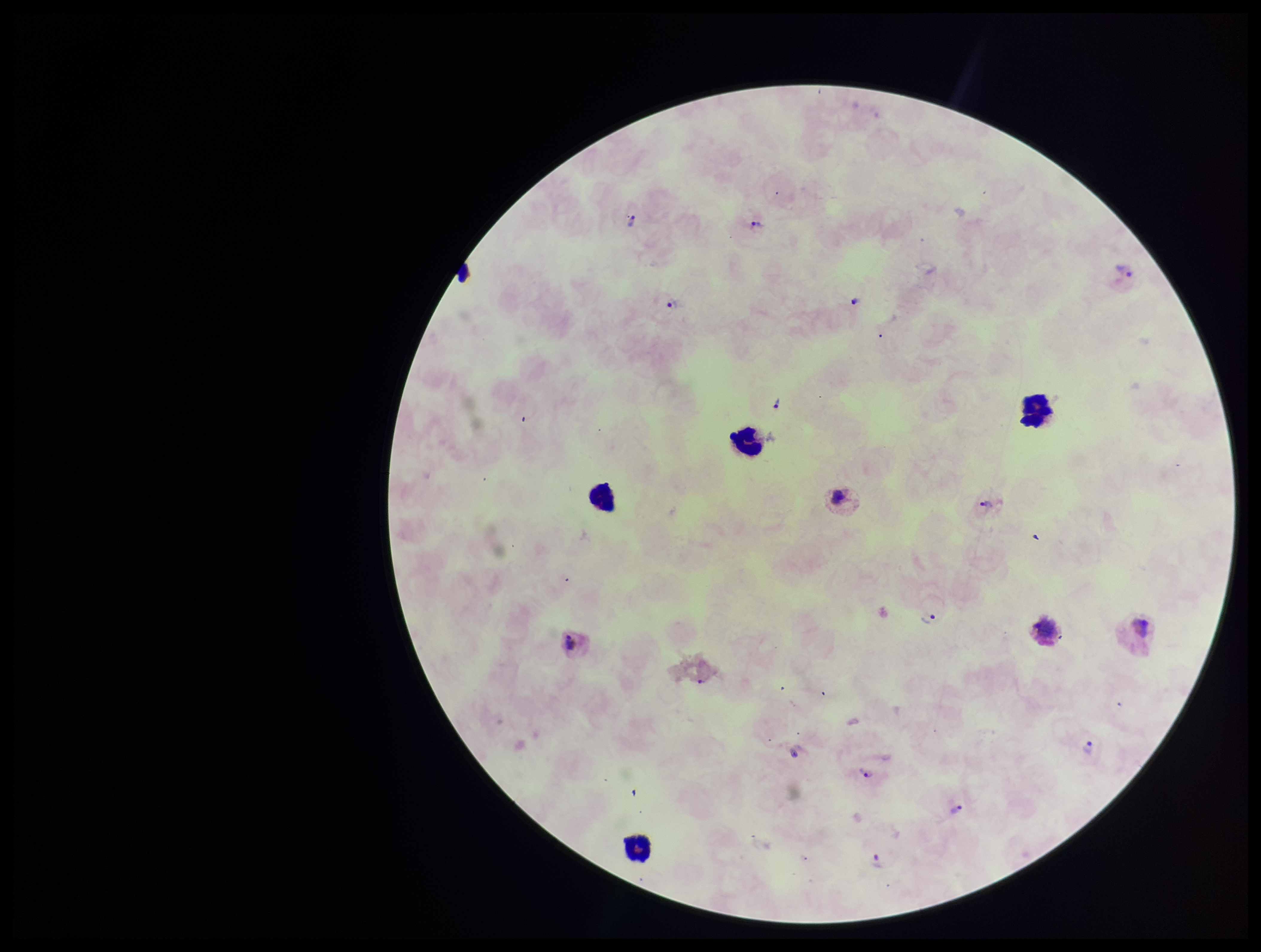

Summary:
  - Leukocyte count: 4
  - Field of view: single
  - Parasite count: 12
  - Plasmodium parasites: identified
  - Patient malaria status: positive
  - Preparation: thick
  - Capture: smartphone photograph through the microscope eyepiece
  - Image size: 1261×952 pixels
  - Stain: Giemsa
  - Species reported for this patient: Plasmodium vivax